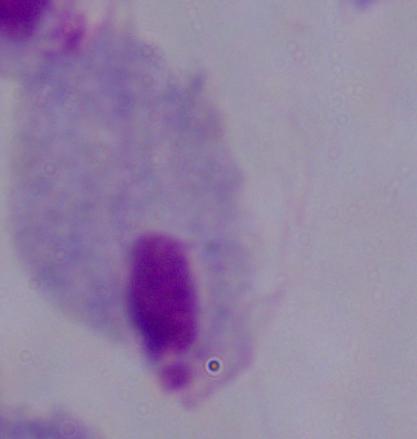
Micrograph. A trichomonad is seen. 1000x magnification.